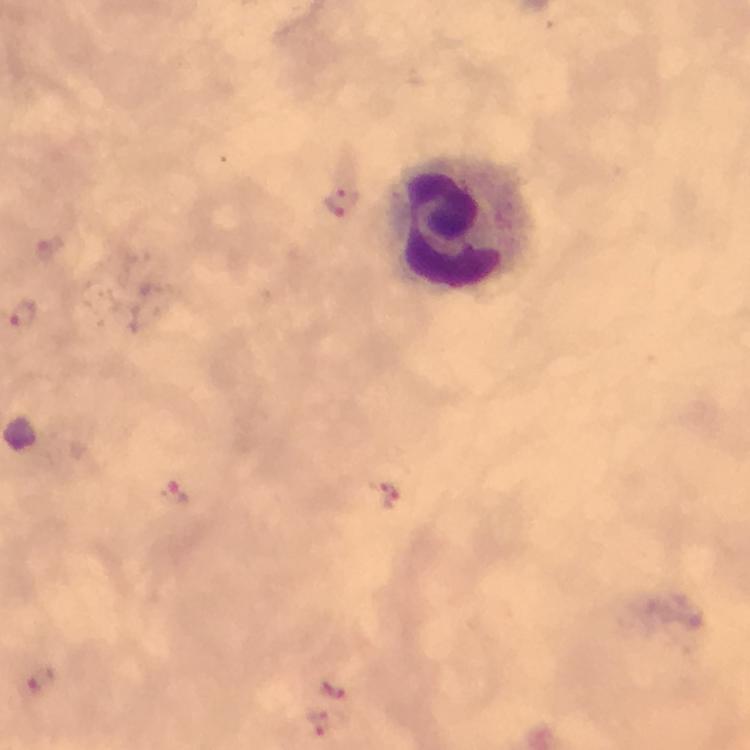

Approximate centers as [x, y] in pixels. Leukocyte locations: [466, 229]. Plasmodium parasite locations: [341, 201], [49, 249], [24, 312], [388, 496], [176, 499], [41, 680], [330, 686], [322, 725]. Giemsa stain. Smartphone photograph taken through a microscope. Cropped region of a single field of view. Immersion oil applied. At 100x magnification. Image is 750×750 pixels. Thick smear. From a malaria diagnostic workup.